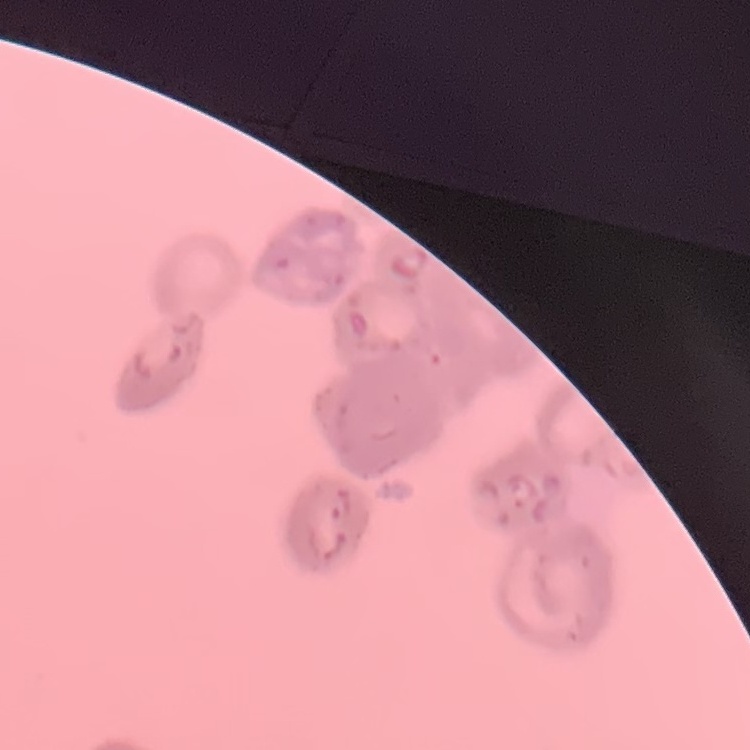

erythrocyte morphology = rouleaux formation
image type = one tile cut from a larger photomicrograph
stain = Field's or Giemsa
preparation = thin blood film